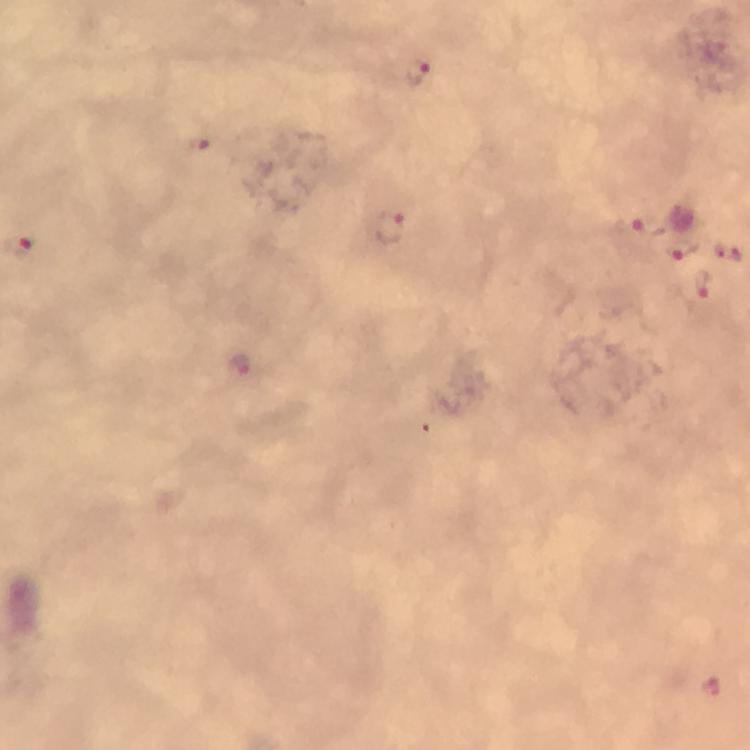 Approximate centers as (x, y) in pixels. Plasmodium parasite locations: (415, 72), (202, 144), (388, 226), (635, 227), (680, 251), (729, 254), (700, 284), (240, 363), (711, 685). Giemsa stain. A crop from one field of view. From a malaria diagnostic workup. Thick blood film. Image is 750×750 pixels. Immersion oil applied. At 100x magnification. Smartphone photograph taken through a microscope.